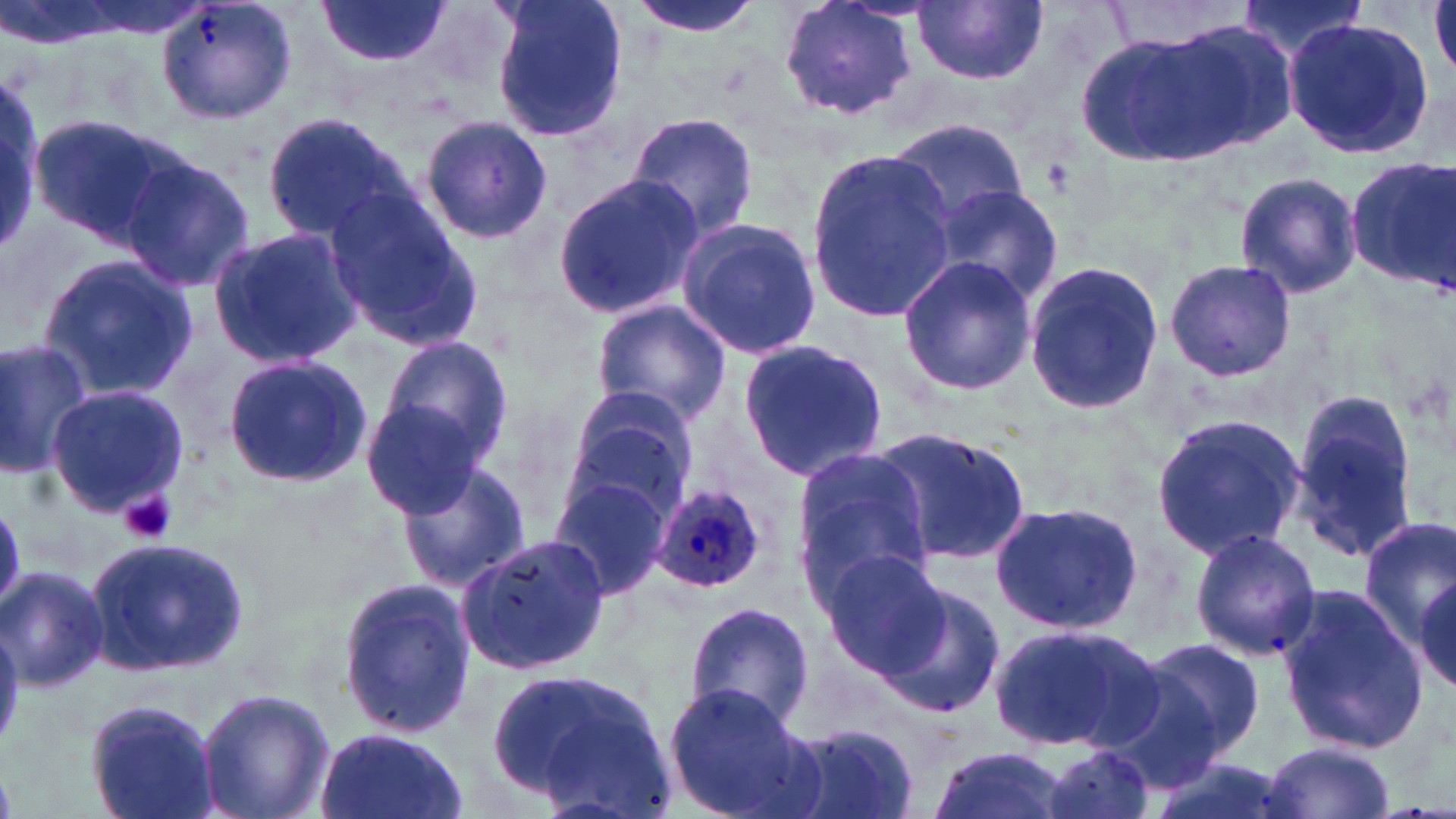
slide-level diagnosis = Plasmodium ovale
platelet locations = approximate bounding boxes as (x1, y1, x2, y2) in pixels: (119, 489, 177, 544)
stain = May-Grünwald-Giemsa
field of view = single
uninfected red blood cell locations = approximate bounding boxes as (x1, y1, x2, y2) in pixels: (155, 0, 300, 127), (314, 0, 451, 68), (487, 0, 629, 144), (626, 0, 765, 39), (776, 0, 921, 121), (1234, 0, 1370, 60), (1103, 1, 1250, 52), (912, 2, 1047, 86), (1131, 15, 1302, 161), (1283, 17, 1434, 161), (1076, 31, 1245, 170), (0, 80, 45, 254), (626, 111, 761, 245), (259, 112, 412, 245), (418, 113, 554, 245), (31, 115, 188, 249), (888, 118, 1029, 230), (805, 148, 957, 325), (119, 155, 256, 292), (1345, 158, 1456, 294), (551, 173, 703, 321), (1234, 173, 1362, 297), (929, 183, 1064, 303), (323, 188, 483, 352), (676, 217, 822, 361), (207, 227, 361, 365), (37, 254, 199, 401), (898, 254, 1035, 397), (1163, 257, 1296, 384), (1023, 259, 1165, 418), (592, 300, 732, 423), (379, 334, 514, 464), (0, 335, 92, 475), (736, 335, 890, 484), (223, 353, 371, 488), (44, 386, 190, 518), (1286, 389, 1422, 564), (557, 390, 697, 525), (359, 399, 490, 517), (1150, 412, 1306, 562), (869, 424, 1031, 567), (790, 448, 934, 600), (396, 458, 532, 593), (548, 469, 675, 600), (988, 497, 1143, 637), (1355, 513, 1456, 651), (1188, 528, 1320, 660), (84, 535, 252, 680), (457, 536, 612, 676), (819, 549, 952, 680), (1, 565, 108, 693), (1405, 566, 1456, 703), (335, 576, 477, 739), (876, 581, 1006, 720), (1275, 590, 1432, 751), (683, 601, 814, 731), (986, 622, 1153, 754), (1124, 633, 1267, 770), (488, 664, 675, 814), (663, 682, 819, 819), (194, 688, 335, 819), (83, 695, 224, 819), (780, 720, 925, 817), (311, 727, 470, 819), (1037, 742, 1159, 819), (1260, 742, 1397, 819), (924, 744, 1072, 819), (1150, 752, 1294, 819)
image size = 1456×819 pixels
magnification = 1000x
modality = light microscopy
preparation = thin blood smear
Plasmodium ovale-infected red blood cell locations = approximate bounding boxes as (x1, y1, x2, y2) in pixels: (649, 483, 774, 592)